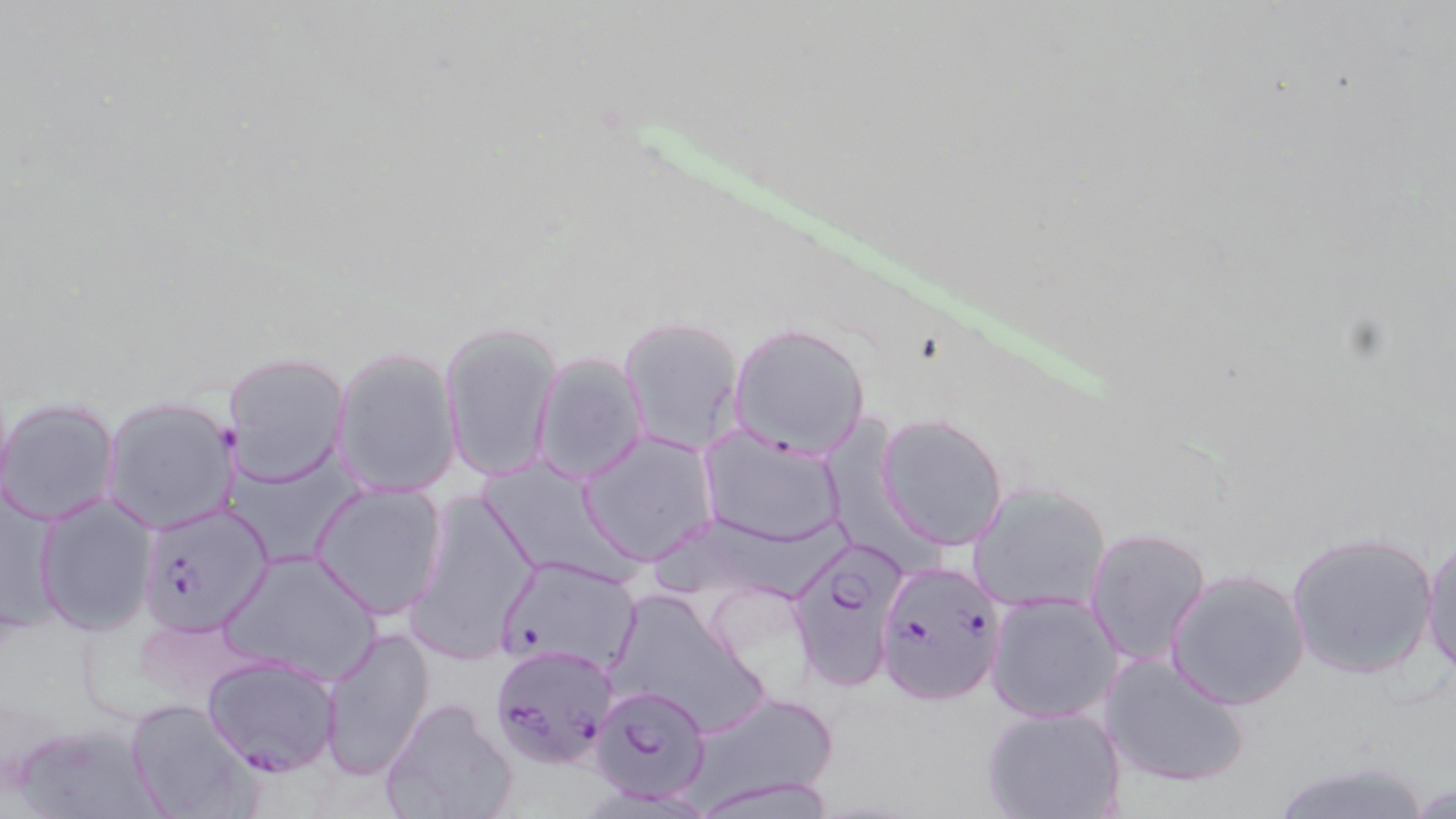
Plasmodium falciparum-infected red blood cell locations = approximate bounding boxes as (x1, y1, x2, y2) in pixels: (137, 504, 273, 635), (785, 537, 909, 693), (878, 565, 1006, 706), (492, 645, 618, 771), (203, 655, 342, 775), (589, 686, 711, 805)
slide-level diagnosis = Plasmodium falciparum
modality = optical microscopy
uninfected red blood cell locations = approximate bounding boxes as (x1, y1, x2, y2) in pixels: (617, 316, 745, 453), (441, 321, 561, 484), (728, 321, 871, 460), (332, 346, 462, 497), (223, 352, 349, 485), (532, 353, 648, 483), (102, 395, 240, 532), (0, 397, 120, 525), (876, 413, 1010, 550), (700, 430, 847, 547), (577, 432, 716, 564), (310, 482, 449, 618), (969, 484, 1111, 612), (406, 489, 540, 660), (34, 493, 159, 633), (1084, 527, 1212, 669), (1286, 530, 1439, 679), (1421, 534, 1456, 678), (222, 547, 381, 683), (494, 557, 642, 673), (1166, 569, 1311, 710), (608, 590, 765, 737), (987, 592, 1122, 723), (320, 627, 434, 778), (1100, 652, 1254, 790), (683, 689, 839, 811), (379, 697, 518, 819), (125, 698, 256, 818), (981, 705, 1125, 819), (11, 718, 169, 819), (1264, 758, 1438, 819)
magnification = 1000x
image size = 1456×819 pixels
preparation = thin blood film
field of view = one of a larger specimen
stain = May-Grünwald-Giemsa